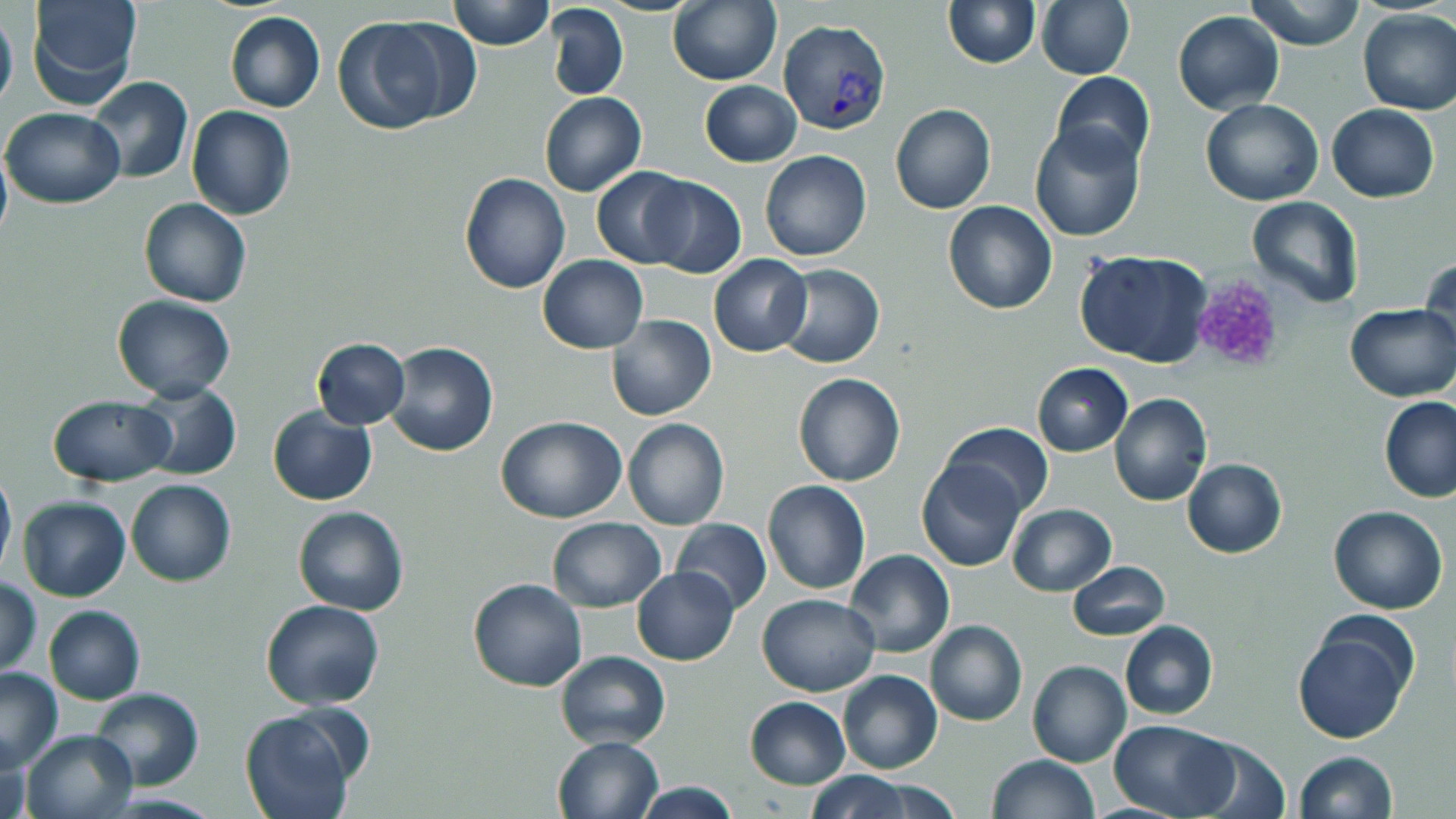

Approximate bounding boxes as named x1/y1/x2/y2 corners in pixels. Plasmodium vivax-infected red blood cell locations: (x1=777, y1=19, x2=891, y2=135). Platelet locations: (x1=1189, y1=275, x2=1288, y2=375). Uninfected red blood cell locations: (x1=24, y1=0, x2=142, y2=108), (x1=447, y1=0, x2=555, y2=50), (x1=667, y1=0, x2=780, y2=86), (x1=1036, y1=0, x2=1134, y2=80), (x1=1247, y1=0, x2=1365, y2=51), (x1=942, y1=1, x2=1040, y2=69), (x1=545, y1=3, x2=629, y2=101), (x1=0, y1=6, x2=17, y2=115), (x1=1357, y1=8, x2=1456, y2=116), (x1=225, y1=11, x2=325, y2=113), (x1=1173, y1=11, x2=1285, y2=114), (x1=332, y1=15, x2=453, y2=135), (x1=1051, y1=70, x2=1155, y2=170), (x1=87, y1=76, x2=194, y2=183), (x1=700, y1=81, x2=801, y2=166), (x1=539, y1=92, x2=646, y2=195), (x1=1200, y1=98, x2=1324, y2=205), (x1=1327, y1=103, x2=1439, y2=201), (x1=891, y1=104, x2=997, y2=214), (x1=186, y1=105, x2=296, y2=220), (x1=3, y1=109, x2=125, y2=208), (x1=1029, y1=122, x2=1145, y2=242), (x1=0, y1=142, x2=11, y2=245), (x1=759, y1=150, x2=872, y2=261), (x1=592, y1=166, x2=694, y2=268), (x1=459, y1=173, x2=571, y2=293), (x1=640, y1=177, x2=747, y2=278), (x1=1246, y1=195, x2=1364, y2=308), (x1=140, y1=197, x2=251, y2=308), (x1=943, y1=201, x2=1057, y2=314), (x1=1074, y1=248, x2=1213, y2=368), (x1=708, y1=253, x2=813, y2=357), (x1=1420, y1=254, x2=1455, y2=358), (x1=538, y1=255, x2=648, y2=353), (x1=775, y1=264, x2=884, y2=368), (x1=112, y1=294, x2=235, y2=402), (x1=1345, y1=303, x2=1456, y2=401), (x1=608, y1=314, x2=715, y2=421), (x1=311, y1=338, x2=410, y2=429), (x1=386, y1=342, x2=498, y2=457), (x1=1029, y1=362, x2=1132, y2=457), (x1=792, y1=373, x2=906, y2=487), (x1=134, y1=381, x2=240, y2=481), (x1=1110, y1=393, x2=1213, y2=507), (x1=48, y1=395, x2=173, y2=486), (x1=1380, y1=397, x2=1456, y2=503), (x1=267, y1=406, x2=377, y2=506), (x1=497, y1=417, x2=624, y2=524), (x1=623, y1=419, x2=730, y2=531), (x1=939, y1=421, x2=1051, y2=518), (x1=916, y1=458, x2=1025, y2=572), (x1=1182, y1=458, x2=1287, y2=559), (x1=0, y1=466, x2=16, y2=579), (x1=126, y1=479, x2=235, y2=586), (x1=762, y1=479, x2=871, y2=596), (x1=18, y1=497, x2=130, y2=602), (x1=1008, y1=503, x2=1115, y2=595), (x1=292, y1=505, x2=410, y2=616), (x1=1328, y1=505, x2=1449, y2=614), (x1=547, y1=517, x2=665, y2=612), (x1=671, y1=519, x2=772, y2=614), (x1=846, y1=549, x2=954, y2=658), (x1=1066, y1=561, x2=1171, y2=640), (x1=632, y1=567, x2=739, y2=664), (x1=468, y1=577, x2=589, y2=692), (x1=1, y1=578, x2=42, y2=678), (x1=757, y1=593, x2=880, y2=697), (x1=260, y1=599, x2=384, y2=711), (x1=44, y1=606, x2=146, y2=704), (x1=925, y1=620, x2=1027, y2=725), (x1=1119, y1=620, x2=1217, y2=721), (x1=1292, y1=621, x2=1415, y2=743), (x1=555, y1=649, x2=670, y2=750), (x1=1027, y1=660, x2=1132, y2=768), (x1=0, y1=666, x2=63, y2=772), (x1=837, y1=670, x2=942, y2=775), (x1=89, y1=687, x2=203, y2=792), (x1=744, y1=696, x2=850, y2=789), (x1=240, y1=706, x2=360, y2=819), (x1=1110, y1=719, x2=1235, y2=817), (x1=20, y1=728, x2=138, y2=819), (x1=1, y1=735, x2=28, y2=819), (x1=552, y1=735, x2=664, y2=819), (x1=1187, y1=736, x2=1291, y2=818), (x1=1294, y1=751, x2=1398, y2=819), (x1=987, y1=754, x2=1098, y2=818), (x1=803, y1=771, x2=919, y2=819), (x1=634, y1=780, x2=741, y2=818). Slide-level diagnosis: Plasmodium vivax. Light microscopy. May-Grünwald-Giemsa-stained preparation. Thin blood smear. 1000x magnification. One field of a larger specimen. Image is 1456×819 pixels.